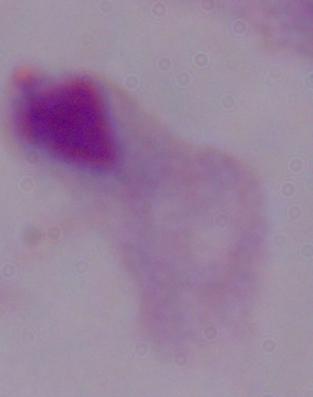

1000x magnification. A trichomonad is seen. Photomicrograph.